Name the blood parasite species.
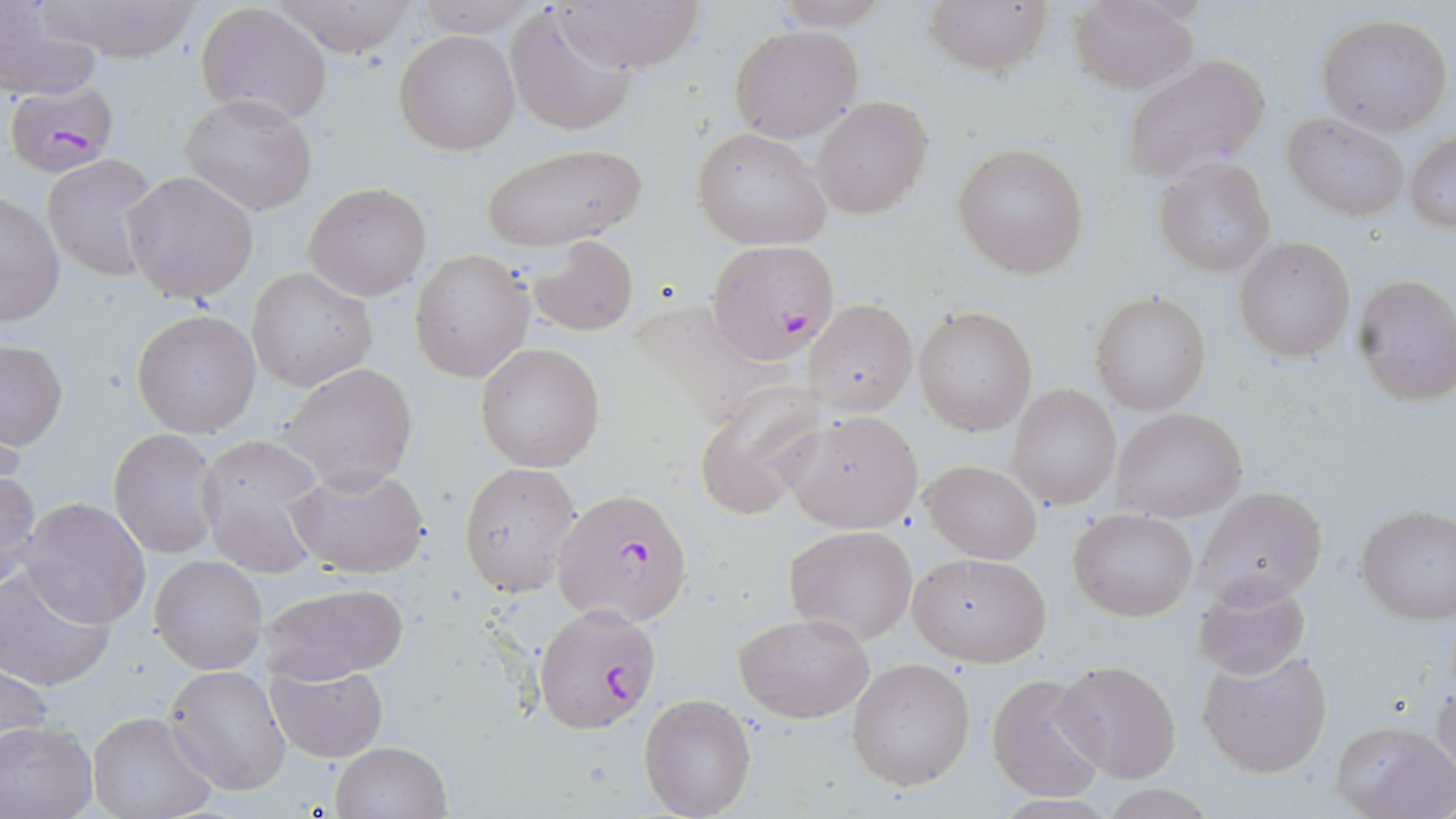
Plasmodium falciparum.

Approximate bounding boxes as [x1, y1, x2, y2] in pixels. Plasmodium falciparum-infected red blood cell locations: [4, 80, 121, 176], [707, 241, 841, 360], [553, 489, 693, 627], [533, 605, 662, 734]. Uninfected red blood cell locations: [34, 0, 205, 62], [410, 0, 545, 37], [554, 0, 701, 75], [771, 0, 896, 29], [924, 0, 1053, 77], [1069, 0, 1199, 94], [270, 1, 413, 58], [195, 2, 332, 124], [0, 3, 103, 103], [505, 6, 636, 135], [1316, 14, 1454, 137], [729, 25, 863, 143], [395, 29, 520, 155], [1120, 54, 1273, 182], [180, 93, 318, 214], [810, 96, 934, 219], [1284, 111, 1410, 221], [691, 128, 831, 249], [1407, 132, 1456, 231], [479, 143, 649, 251], [953, 143, 1090, 277], [42, 154, 163, 281], [1154, 159, 1276, 275], [123, 170, 259, 303], [303, 181, 432, 301], [1, 193, 66, 325], [528, 236, 639, 336], [1235, 238, 1356, 361], [410, 250, 534, 383], [247, 267, 377, 392], [1352, 273, 1456, 404], [1091, 292, 1210, 414], [805, 300, 916, 417], [914, 306, 1037, 434], [131, 310, 261, 437], [0, 340, 68, 450], [474, 341, 605, 472], [279, 363, 418, 490], [694, 384, 828, 521], [1010, 385, 1120, 509], [1112, 408, 1248, 523], [785, 411, 922, 533], [110, 427, 224, 559], [194, 435, 329, 574], [922, 459, 1043, 565], [458, 462, 582, 596], [285, 463, 429, 579], [0, 468, 40, 589], [1198, 485, 1328, 607], [17, 497, 150, 628], [1356, 504, 1456, 626], [1069, 508, 1198, 621], [785, 525, 916, 643], [906, 552, 1053, 667], [151, 554, 268, 673], [0, 565, 115, 691], [1192, 575, 1313, 680], [258, 579, 411, 686], [734, 612, 875, 723], [1196, 648, 1333, 779], [846, 657, 976, 792], [1, 660, 54, 756], [1054, 660, 1183, 784], [164, 664, 291, 796], [264, 664, 387, 763], [985, 672, 1109, 803], [1431, 684, 1456, 786], [638, 693, 757, 819], [86, 710, 217, 819], [1330, 719, 1455, 819], [0, 721, 97, 819], [331, 741, 451, 818]. Image is 1456×819 pixels. One field of a larger specimen. May-Grünwald-Giemsa-stained preparation. Optical microscopy. Thin blood film. Captured at 1000x magnification.